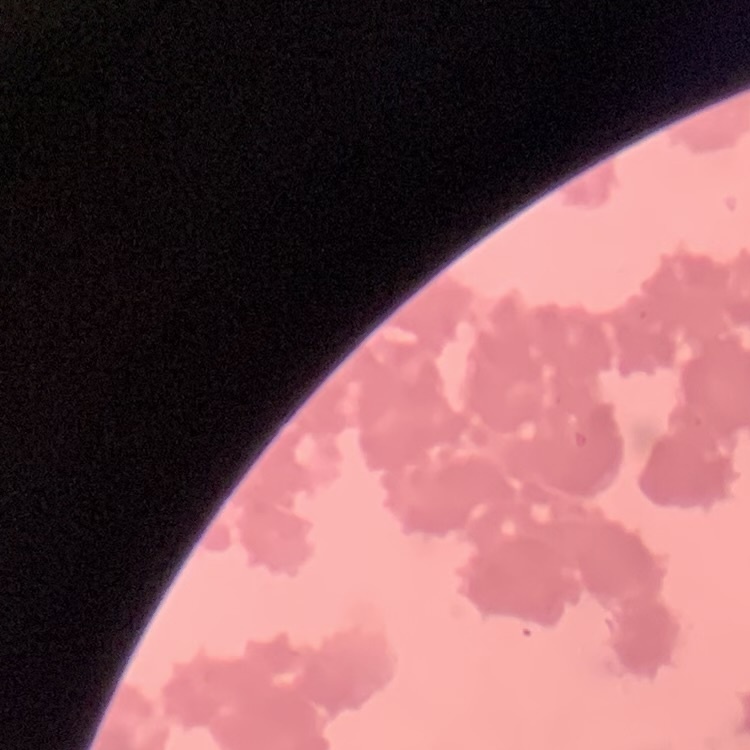

The red blood cells show rouleaux formation. Field's or Giemsa stain. Thin blood film. Square crop of a larger photomicrograph.